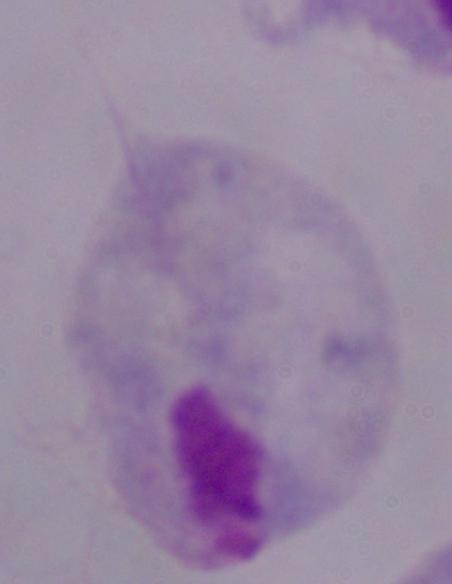
1000x magnification. Micrograph. A trichomonad is seen.